Classify this cell by malaria status.
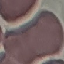
It is uninfected.

Acquired by smartphone through the microscope eyepiece. Thin blood smear. Cell patch, automatically extracted from a larger field of view and resized to 64 × 64 pixels. Giemsa-stained preparation.